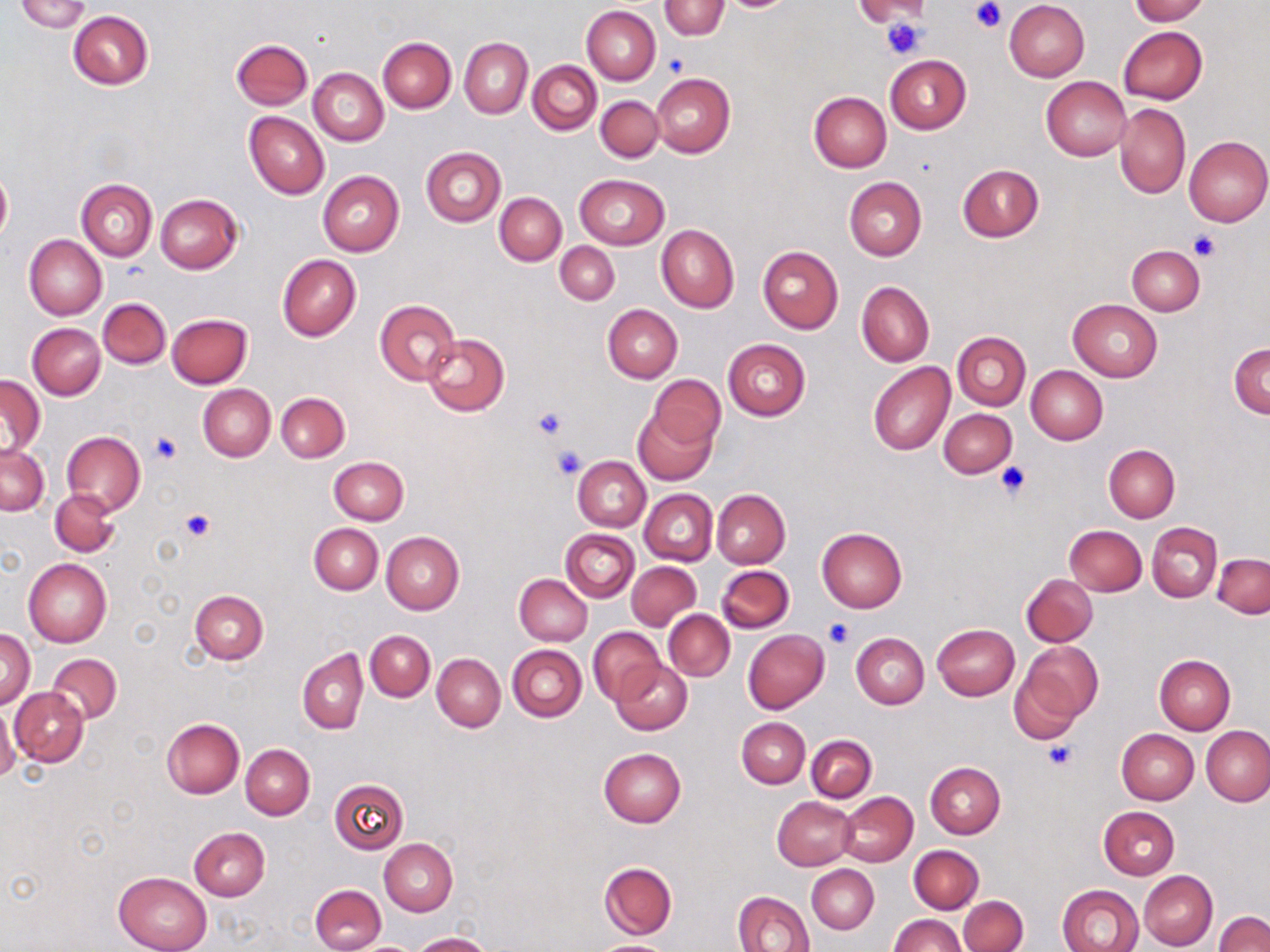

slide-level diagnosis = no evidence of blood parasites
stain = May-Grünwald-Giemsa
magnification = 1000x
field of view = one of a larger specimen
modality = light microscopy
preparation = thin blood smear
uninfected red blood cell locations = approximate bounding boxes as (x1, y1, x2, y2) in pixels: (12, 0, 89, 32), (1128, 0, 1209, 24), (660, 1, 729, 39), (721, 1, 792, 11), (855, 1, 930, 24), (1004, 1, 1090, 81), (582, 6, 661, 85), (68, 12, 154, 90), (1119, 26, 1207, 103), (378, 36, 456, 113), (231, 38, 313, 110), (459, 38, 533, 119), (885, 54, 971, 133), (528, 61, 602, 135), (308, 69, 388, 146), (652, 73, 734, 157), (1040, 76, 1131, 161), (809, 91, 892, 172), (596, 96, 663, 163), (1115, 102, 1190, 199), (244, 111, 329, 199), (1184, 136, 1269, 226), (422, 147, 506, 227), (957, 163, 1044, 242), (0, 165, 11, 247), (318, 171, 404, 256), (575, 175, 669, 249), (844, 177, 926, 260), (76, 178, 157, 260), (495, 192, 566, 265), (155, 193, 242, 273), (656, 224, 739, 312), (24, 235, 107, 319), (555, 242, 619, 305), (758, 245, 843, 335), (1125, 245, 1205, 316), (277, 254, 360, 341), (856, 281, 934, 366), (98, 297, 170, 369), (375, 299, 460, 386), (1069, 300, 1161, 381), (603, 305, 682, 382), (167, 313, 252, 388), (28, 323, 105, 399), (953, 331, 1030, 410), (422, 333, 509, 416), (722, 338, 810, 421), (1229, 342, 1269, 419), (868, 362, 955, 455), (1027, 366, 1107, 444), (648, 375, 724, 452), (1, 376, 44, 458), (197, 385, 275, 462), (276, 391, 349, 462), (634, 407, 717, 485), (939, 408, 1017, 477), (61, 432, 145, 516), (1, 444, 48, 516), (1104, 444, 1180, 523), (330, 456, 408, 524), (573, 457, 651, 531), (51, 488, 120, 558), (712, 489, 790, 568), (640, 490, 717, 565), (1148, 522, 1222, 601), (309, 524, 382, 595), (1064, 525, 1147, 596), (817, 526, 907, 612), (561, 529, 639, 601), (382, 532, 464, 615), (1213, 553, 1269, 618), (24, 557, 111, 646), (626, 562, 701, 631), (716, 564, 794, 633), (514, 574, 592, 645), (1022, 574, 1098, 646), (189, 589, 268, 663), (664, 610, 734, 681), (932, 624, 1020, 700), (587, 627, 665, 704), (0, 630, 35, 708), (365, 630, 435, 701), (743, 630, 829, 713), (852, 633, 929, 709), (1017, 639, 1102, 728), (507, 645, 587, 722), (298, 648, 368, 733), (47, 653, 121, 724), (433, 654, 505, 731), (1155, 655, 1235, 734), (612, 659, 692, 735), (10, 688, 88, 767), (0, 703, 19, 785), (736, 717, 810, 788), (161, 718, 243, 798), (1202, 726, 1270, 805), (1117, 729, 1198, 805), (806, 734, 876, 802), (241, 745, 314, 819), (598, 747, 686, 827), (925, 762, 1004, 839), (329, 778, 408, 854), (838, 791, 917, 866), (772, 797, 857, 870), (1098, 807, 1179, 880), (189, 826, 270, 901), (380, 838, 456, 915), (908, 845, 983, 913), (600, 862, 677, 938), (807, 865, 879, 934), (1139, 870, 1218, 950), (114, 871, 212, 952), (310, 883, 385, 952), (1057, 885, 1143, 952), (733, 890, 814, 952), (958, 896, 1027, 952), (1214, 911, 1270, 952), (890, 914, 966, 952), (410, 931, 491, 952), (592, 939, 676, 952), (356, 942, 419, 952)
image size = 1270×952 pixels
platelet locations = approximate bounding boxes as (x1, y1, x2, y2) in pixels: (971, 0, 1005, 34), (881, 18, 926, 60), (664, 54, 689, 76), (1188, 231, 1221, 262), (532, 407, 568, 440), (150, 433, 181, 463), (551, 443, 588, 480), (994, 460, 1032, 501), (181, 510, 215, 541), (824, 617, 854, 647), (1042, 741, 1078, 771)